Identify the cell.
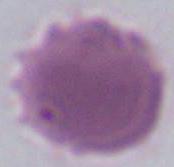

This is an erythrocyte.

modality: micrograph
magnification: 1000x